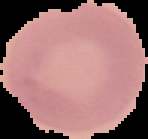

image type = segmented cell region with the area outside set to black
malaria status = uninfected
preparation = thin blood smear
image size = 148×139 pixels